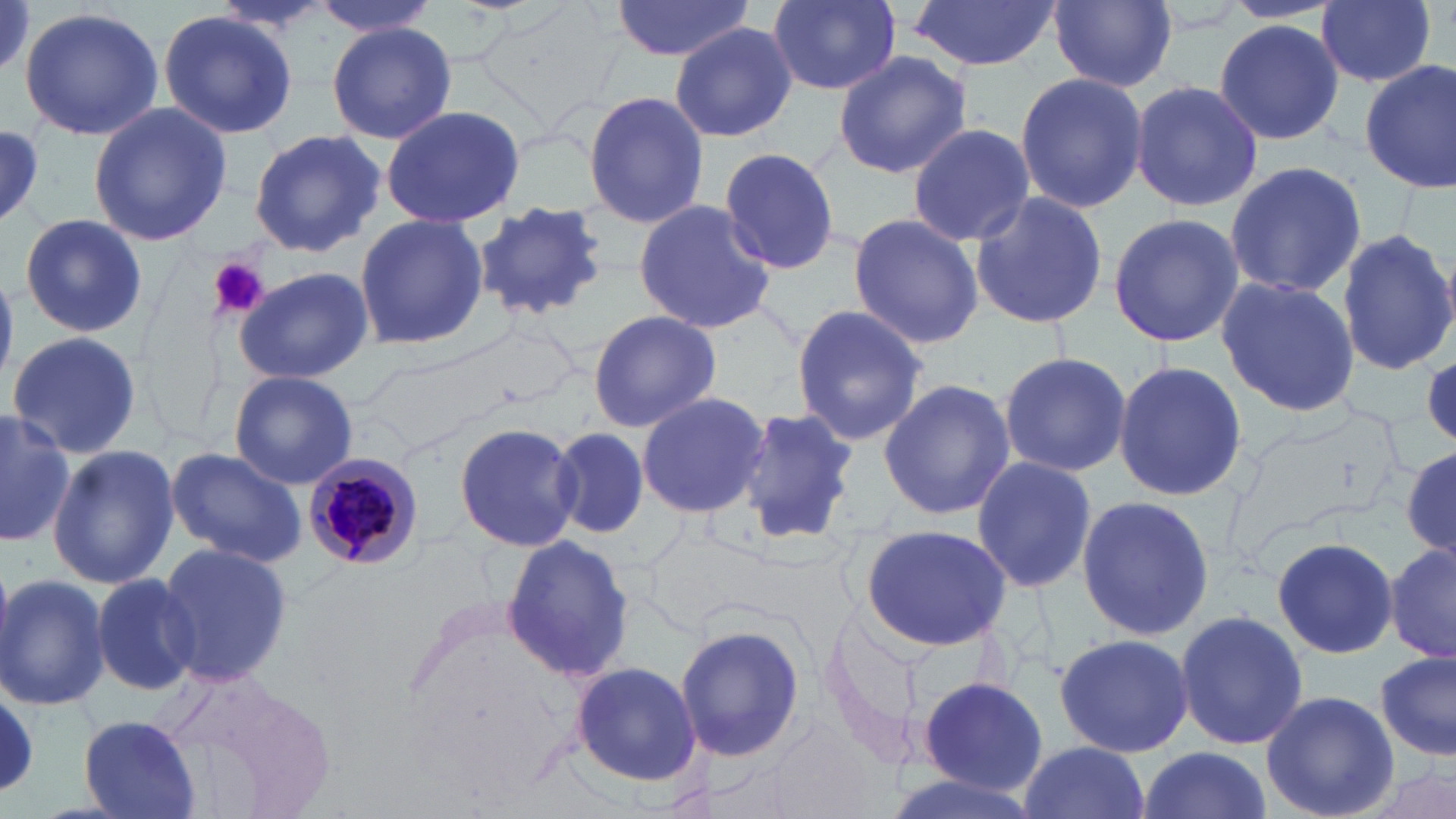

Summary:
  - Coordinate format: approximate bounding boxes as named x1/y1/x2/y2 corners in pixels
  - Uninfected red blood cell locations: (x1=311, y1=0, x2=444, y2=36), (x1=610, y1=0, x2=755, y2=62), (x1=765, y1=0, x2=901, y2=95), (x1=908, y1=0, x2=1059, y2=71), (x1=1051, y1=0, x2=1177, y2=91), (x1=1317, y1=0, x2=1436, y2=88), (x1=18, y1=6, x2=165, y2=141), (x1=160, y1=11, x2=297, y2=139), (x1=1211, y1=20, x2=1345, y2=146), (x1=670, y1=21, x2=797, y2=140), (x1=328, y1=22, x2=456, y2=145), (x1=831, y1=50, x2=971, y2=179), (x1=1358, y1=60, x2=1456, y2=194), (x1=1014, y1=71, x2=1147, y2=214), (x1=1128, y1=80, x2=1263, y2=212), (x1=582, y1=90, x2=709, y2=232), (x1=87, y1=101, x2=231, y2=248), (x1=379, y1=103, x2=525, y2=230), (x1=906, y1=122, x2=1034, y2=245), (x1=0, y1=124, x2=45, y2=221), (x1=247, y1=129, x2=387, y2=256), (x1=717, y1=146, x2=845, y2=276), (x1=1225, y1=160, x2=1366, y2=299), (x1=968, y1=190, x2=1109, y2=330), (x1=630, y1=197, x2=776, y2=335), (x1=471, y1=200, x2=610, y2=324), (x1=1106, y1=211, x2=1244, y2=350), (x1=354, y1=212, x2=487, y2=353), (x1=846, y1=213, x2=986, y2=350), (x1=19, y1=214, x2=145, y2=337), (x1=1336, y1=229, x2=1455, y2=378), (x1=231, y1=267, x2=373, y2=386), (x1=1214, y1=276, x2=1359, y2=419), (x1=790, y1=303, x2=927, y2=447), (x1=586, y1=309, x2=720, y2=433), (x1=6, y1=331, x2=144, y2=462), (x1=371, y1=332, x2=547, y2=451), (x1=998, y1=350, x2=1132, y2=477), (x1=1424, y1=354, x2=1456, y2=445), (x1=1112, y1=359, x2=1247, y2=503), (x1=229, y1=371, x2=360, y2=490), (x1=878, y1=377, x2=1016, y2=520), (x1=635, y1=390, x2=771, y2=520), (x1=732, y1=407, x2=860, y2=546), (x1=0, y1=409, x2=77, y2=546), (x1=453, y1=420, x2=583, y2=554), (x1=551, y1=427, x2=648, y2=538), (x1=48, y1=444, x2=181, y2=588), (x1=166, y1=447, x2=306, y2=568), (x1=1402, y1=447, x2=1456, y2=557), (x1=970, y1=456, x2=1097, y2=595), (x1=1075, y1=495, x2=1215, y2=641), (x1=859, y1=523, x2=1009, y2=651), (x1=1271, y1=535, x2=1399, y2=661), (x1=504, y1=536, x2=634, y2=683), (x1=1386, y1=542, x2=1454, y2=666), (x1=155, y1=543, x2=293, y2=688), (x1=0, y1=571, x2=110, y2=714), (x1=91, y1=572, x2=202, y2=696), (x1=1173, y1=608, x2=1309, y2=753), (x1=673, y1=621, x2=808, y2=763), (x1=1051, y1=630, x2=1193, y2=756), (x1=1375, y1=653, x2=1455, y2=761), (x1=571, y1=661, x2=702, y2=785), (x1=912, y1=676, x2=1051, y2=796), (x1=0, y1=689, x2=41, y2=795), (x1=1261, y1=690, x2=1398, y2=819), (x1=78, y1=715, x2=203, y2=817), (x1=1018, y1=741, x2=1151, y2=819), (x1=1137, y1=744, x2=1272, y2=819)
  - Platelet locations: (x1=207, y1=257, x2=269, y2=318)
  - Plasmodium malariae-infected red blood cell locations: (x1=301, y1=451, x2=426, y2=572)
  - Slide-level diagnosis: Plasmodium malariae
  - Stain: May-Grünwald-Giemsa
  - Image size: 1456×819 pixels
  - Preparation: thin blood film
  - Field of view: single
  - Magnification: 1000x
  - Modality: light microscopy